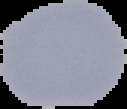

preparation = thin blood film
image type = cell region segmented out of the field of view; surrounding area masked to black
image size = 127×109 pixels
malaria status = uninfected